Assess this cell for malaria.
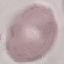
It is uninfected.

preparation = thin blood smear
stain = Giemsa
image type = cell patch, automatically extracted from a larger field of view and resized to 64 × 64 pixels
capture = smartphone through the microscope eyepiece